Report the malaria status of this cell.
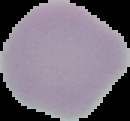

Uninfected.

image size = 130×121 pixels
image type = segmented cell region with the area outside set to black
preparation = thin blood film